Point out Plasmodium parasites and leukocytes.
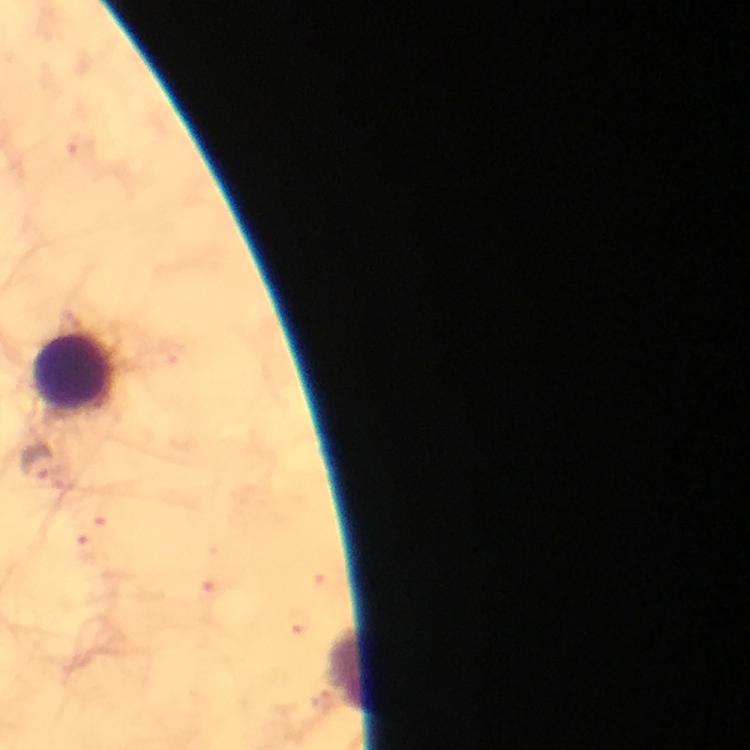

Approximate centers as {x, y} in pixels.
Plasmodium parasites: {36, 463}.
Leukocytes: {76, 372}, {346, 667}.

image size = 750×750 pixels
immersion oil = used
capture = smartphone mounted on the microscope
preparation = thick smear
stain = Giemsa
magnification = 100x
context = from a malaria diagnostic workup
cropped from = a single field of view